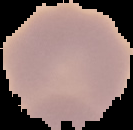

Cell region segmented out of the field of view; the surrounding area is masked to black. Image is 133×130 pixels. Result: negative for Plasmodium parasites. From a thin blood smear.